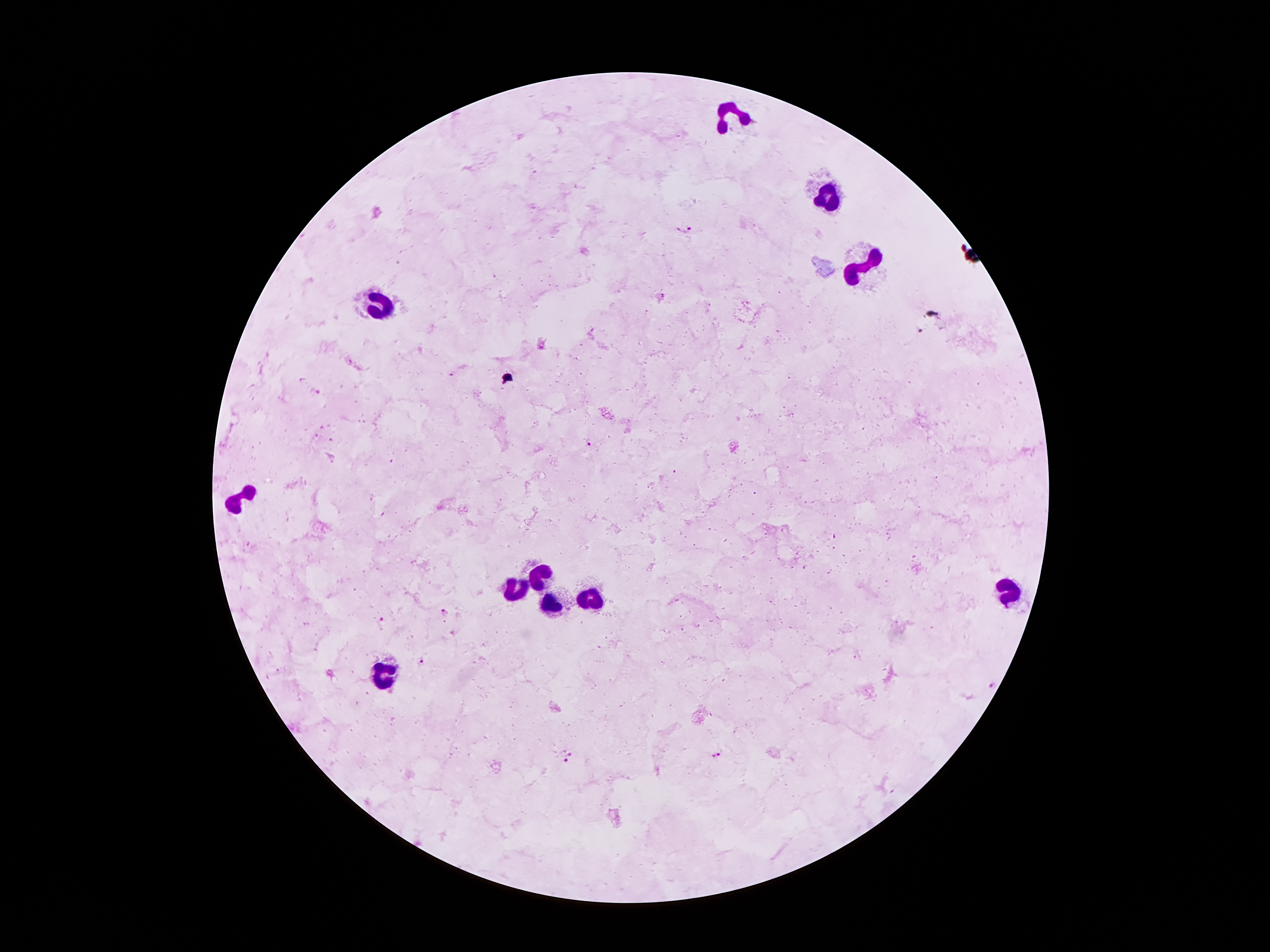
{
  "stain": "Giemsa",
  "capture": "smartphone camera through the microscope eyepiece",
  "magnification": "100x",
  "malaria_parasite_locations": "approximate centers as (x, y) in pixels: (684, 227), (922, 330), (587, 441), (445, 612), (381, 620), (422, 662), (993, 684), (569, 753), (717, 755), (564, 762)",
  "patient_malaria_status": "infected with Plasmodium falciparum",
  "preparation": "thick blood smear",
  "field_of_view": "single",
  "image_size": "1270×952 pixels",
  "leukocyte_locations": "approximate centers as (x, y) in pixels: (733, 113), (831, 195), (863, 265), (380, 306), (243, 494), (543, 577), (515, 587), (1008, 592), (586, 598), (553, 606), (380, 678)"
}